Locate and identify every blood parasite.
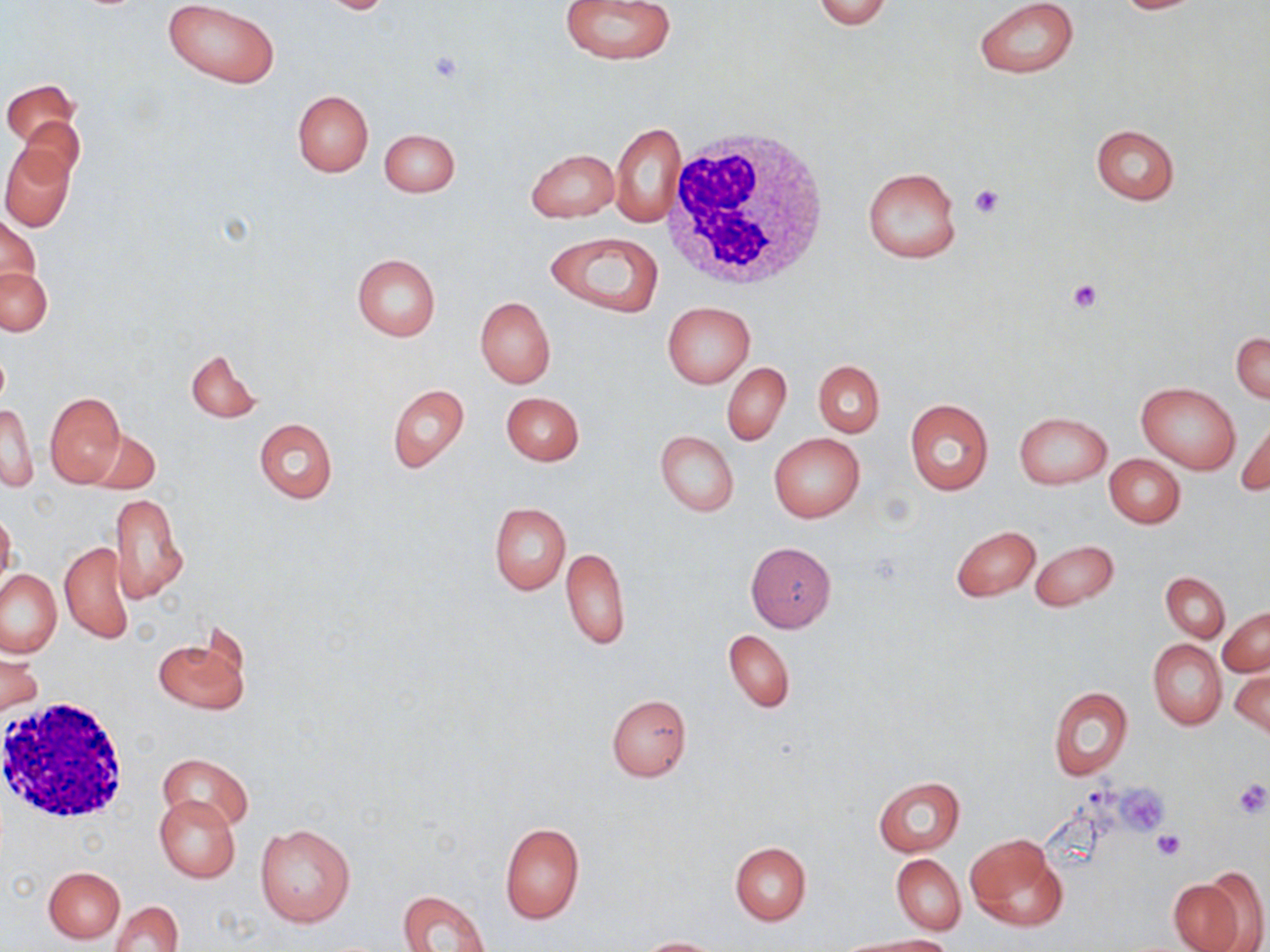
No blood parasites observed.

Summary:
  - Coordinate format: approximate bounding boxes as [x1, y1, x2, y2] in pixels
  - Uninfected red blood cell locations: [558, 0, 676, 65], [812, 0, 892, 29], [973, 0, 1079, 78], [1109, 0, 1206, 14], [162, 1, 280, 88], [313, 1, 398, 14], [2, 79, 79, 147], [291, 89, 374, 176], [15, 114, 86, 184], [609, 123, 684, 228], [1090, 123, 1181, 205], [379, 128, 460, 197], [538, 133, 678, 225], [1, 146, 75, 231], [527, 148, 618, 223], [862, 166, 962, 265], [0, 216, 40, 299], [545, 231, 664, 318], [351, 253, 441, 340], [0, 267, 52, 336], [475, 296, 555, 389], [663, 302, 754, 387], [1232, 332, 1270, 403], [186, 349, 260, 422], [813, 361, 884, 437], [721, 362, 791, 446], [1137, 382, 1241, 473], [387, 384, 470, 473], [501, 391, 584, 467], [44, 393, 127, 487], [905, 398, 993, 497], [1, 404, 38, 492], [1014, 411, 1111, 488], [1236, 417, 1270, 497], [254, 419, 337, 504], [86, 424, 160, 492], [654, 429, 738, 517], [769, 432, 865, 523], [1105, 454, 1184, 528], [109, 493, 187, 601], [489, 501, 571, 596], [0, 509, 17, 593], [951, 525, 1041, 602], [59, 539, 134, 643], [1030, 539, 1119, 613], [745, 542, 837, 632], [559, 546, 631, 651], [0, 569, 63, 659], [1161, 573, 1229, 641], [1219, 606, 1269, 677], [724, 630, 795, 712], [154, 631, 250, 715], [1147, 639, 1226, 730], [0, 650, 43, 716], [1231, 667, 1270, 739], [1048, 687, 1133, 782], [606, 693, 692, 780], [159, 753, 252, 833], [873, 776, 965, 857], [154, 795, 239, 882], [499, 821, 585, 925], [255, 823, 356, 928], [965, 834, 1067, 933], [731, 842, 811, 925], [891, 853, 965, 935], [43, 866, 125, 943], [1167, 874, 1250, 952], [398, 888, 492, 952], [110, 900, 183, 952], [843, 935, 954, 951], [636, 937, 723, 951]
  - White blood cell locations: [660, 128, 833, 290], [1, 697, 131, 824]
  - Platelet locations: [427, 50, 465, 84], [969, 185, 1002, 218], [1067, 280, 1102, 313], [1231, 779, 1270, 818], [1119, 787, 1166, 832], [1153, 829, 1187, 860]
  - Slide-level diagnosis: no evidence of blood parasites
  - Stain: May-Grünwald-Giemsa
  - Magnification: 1000x
  - Image size: 1270×952 pixels
  - Modality: light microscopy
  - Preparation: thin blood smear
  - Field of view: one of a larger specimen